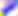

magnification = 400x
modality = photomicrograph
identification = Toxoplasma gondii